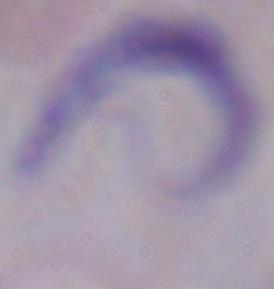

magnification = 1000x
modality = micrograph
identification = trypanosome